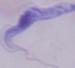

A trypanosome is seen. 1000x magnification. Photomicrograph.